Point out every Plasmodium parasite.
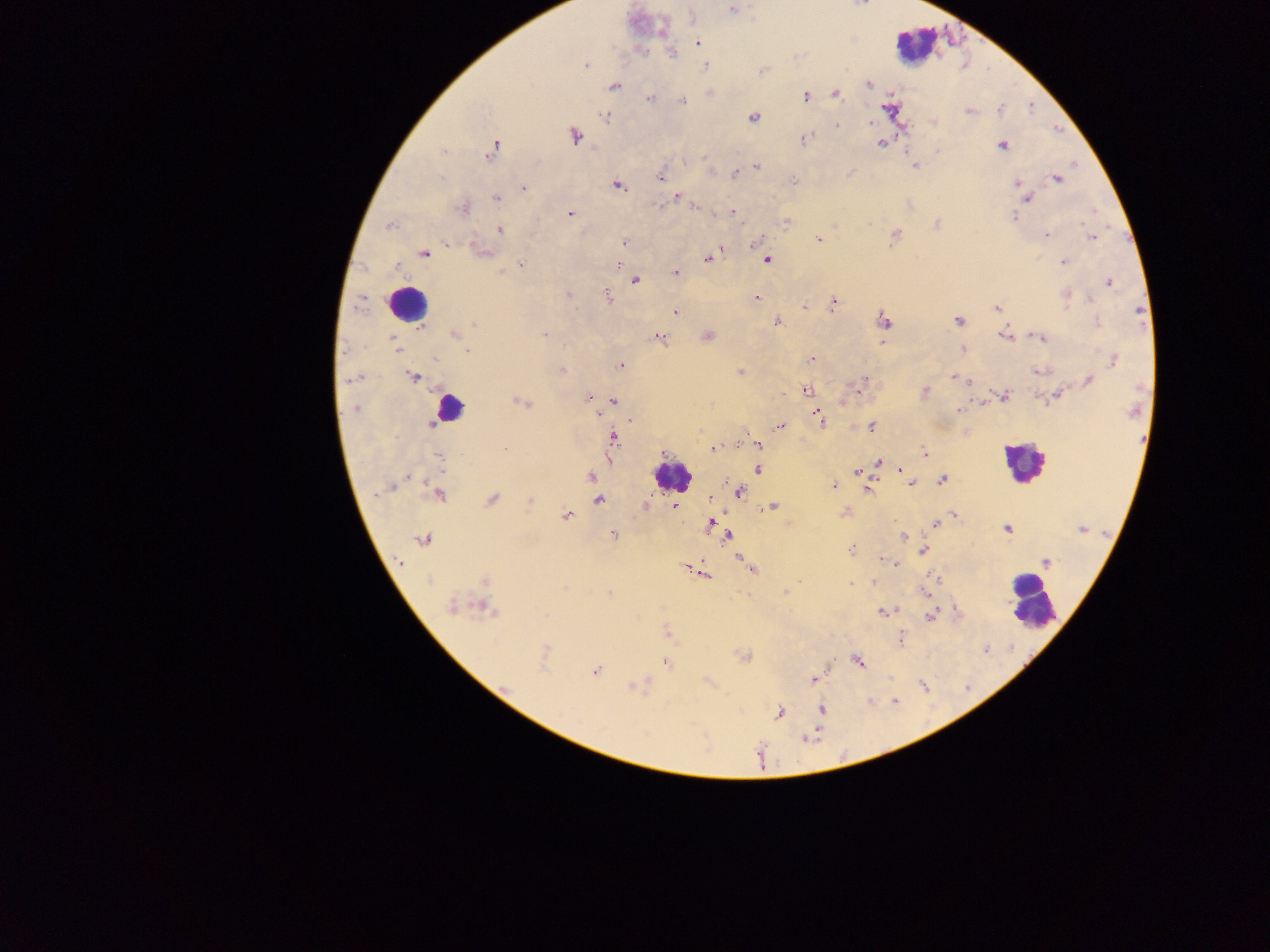

Approximate centers as (x, y) in pixels.
Plasmodium parasites: (732, 9), (697, 41), (671, 52), (586, 65), (705, 65), (763, 71), (869, 84), (613, 86), (835, 94), (806, 96), (650, 98), (683, 101), (999, 108), (969, 111), (605, 116), (753, 118), (870, 123), (837, 125), (574, 136), (804, 140), (880, 143), (1002, 146), (492, 149), (444, 151), (938, 151), (704, 157), (685, 161), (914, 166), (756, 167), (735, 174), (661, 177), (440, 178), (1057, 178), (794, 181), (1017, 184), (617, 186), (523, 188), (1020, 188), (677, 197), (1027, 197), (497, 198), (659, 206), (695, 206), (462, 208), (733, 212), (570, 214), (1013, 217), (936, 225), (390, 226), (499, 230), (1046, 236), (894, 237), (818, 238), (1092, 238), (757, 241), (624, 242), (446, 244), (481, 253), (424, 254), (708, 259), (767, 260), (1064, 263), (521, 264), (618, 264), (501, 272), (676, 273), (634, 281), (1109, 283), (568, 294), (1065, 295), (609, 298), (756, 299), (359, 303), (833, 304), (804, 306), (997, 308), (675, 312), (1139, 312), (957, 320), (884, 321), (778, 322), (1097, 323), (474, 324), (419, 329), (454, 334), (544, 334), (707, 335), (1005, 335), (392, 337), (659, 337), (1040, 337), (883, 343), (395, 345), (398, 349), (963, 349), (467, 351), (433, 358), (811, 360), (1114, 360), (621, 365), (561, 370), (1039, 371), (740, 372), (414, 377), (954, 378), (348, 379), (864, 380), (1088, 381), (861, 388), (805, 390), (924, 392), (1003, 396), (1055, 396), (589, 398), (614, 401), (522, 403), (355, 409), (959, 410), (597, 413), (819, 418), (779, 426), (871, 427), (614, 438), (757, 445), (714, 448), (506, 450), (924, 453), (440, 458), (878, 461), (758, 468), (901, 470), (856, 472), (907, 476), (408, 477), (591, 477), (942, 480), (911, 483), (395, 484), (834, 485), (390, 487), (869, 490), (738, 492), (437, 495), (710, 498), (599, 499), (491, 500), (530, 500), (676, 506), (773, 506), (844, 513), (567, 515), (954, 515), (711, 524), (935, 525), (1007, 529), (1082, 529), (612, 534), (728, 535), (904, 537), (423, 540), (851, 549), (923, 550), (883, 559), (740, 560), (399, 561), (893, 563), (1046, 563), (750, 568), (701, 572), (429, 580), (484, 580), (874, 582), (851, 584), (564, 587), (786, 591), (609, 593), (450, 608), (484, 609), (884, 612), (931, 616), (668, 632), (901, 638), (743, 657), (857, 661), (665, 662), (595, 671), (814, 680), (633, 687), (821, 710), (779, 713), (807, 738).

Leukocyte locations: (915, 45), (408, 303), (447, 409), (1023, 462), (671, 477), (1031, 602). Mobile-phone photograph taken through the microscope. One field of view. Thick blood smear. Image is 1270×952 pixels. Sample from Ghana.